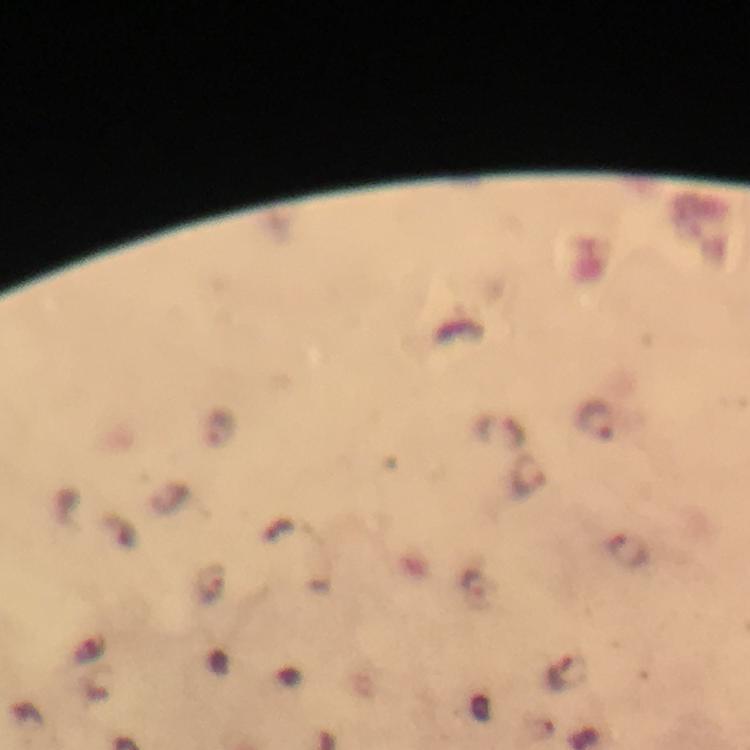 Approximate centers as {x, y} in pixels. Malaria parasite locations: {595, 420}, {530, 476}, {629, 550}, {211, 585}, {475, 590}, {565, 671}. From a malaria diagnostic workup. Thick blood smear. A crop from one field of view. Giemsa-stained preparation. Image is 750×750 pixels. Immersion oil was used. 100x magnification. Photographed through the microscope with a smartphone camera.